Assess the morphology of the red blood cells.
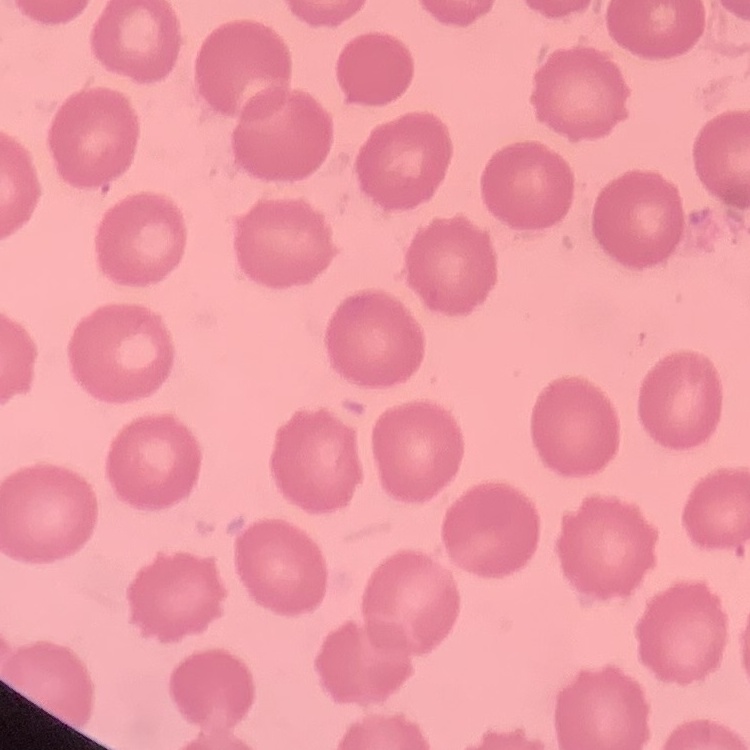

No rouleaux formation.

Summary:
  - Stain: Field's or Giemsa
  - Preparation: thin peripheral smear
  - Image type: one tile cut from a larger photomicrograph